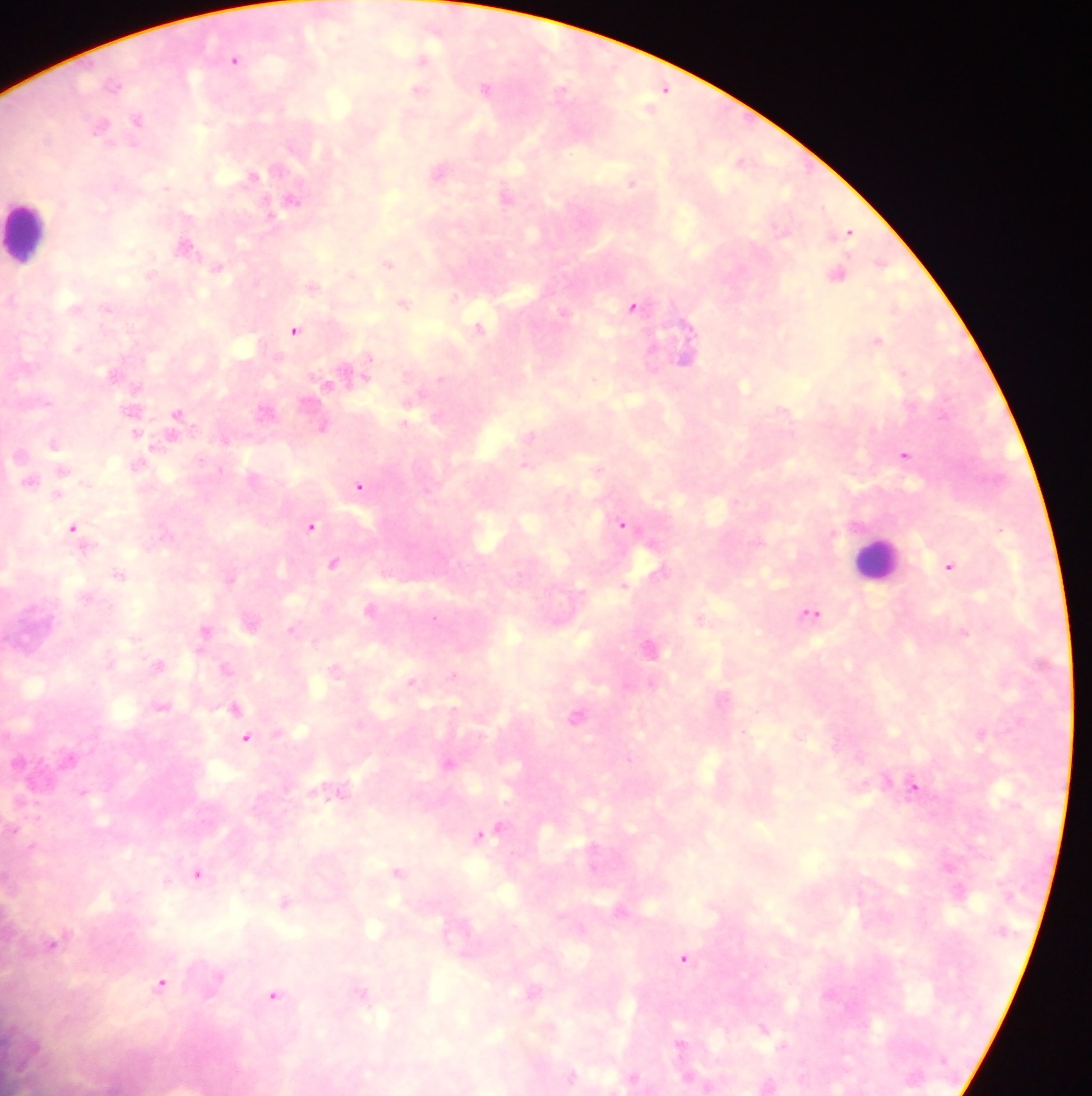
Approximate centers as [x, y] in pixels. Leukocyte locations: [25, 231], [877, 556]. Malaria parasite locations: [234, 59], [422, 60], [113, 84], [485, 88], [562, 89], [663, 89], [417, 90], [137, 119], [100, 125], [47, 138], [739, 161], [438, 171], [253, 175], [630, 183], [505, 196], [292, 199], [848, 232], [187, 246], [387, 263], [217, 268], [151, 274], [837, 274], [313, 285], [404, 303], [633, 306], [74, 307], [107, 308], [563, 312], [478, 326], [295, 330], [876, 340], [78, 348], [366, 362], [347, 372], [113, 374], [325, 384], [745, 386], [137, 388], [264, 410], [176, 414], [323, 427], [135, 433], [530, 435], [54, 444], [903, 454], [524, 465], [62, 471], [30, 481], [359, 486], [57, 495], [623, 524], [310, 526], [73, 528], [333, 562], [949, 566], [657, 570], [119, 575], [229, 579], [810, 614], [434, 617], [292, 629], [205, 630], [963, 632], [649, 647], [158, 665], [225, 668], [411, 680], [721, 698], [161, 706], [233, 708], [575, 715], [240, 718], [979, 733], [246, 738], [448, 763], [913, 787], [488, 832], [397, 872], [199, 875], [284, 902], [619, 909], [52, 944], [683, 959], [161, 983], [532, 991], [273, 996], [763, 1028], [678, 1044], [571, 1076], [633, 1077]. Sample from Ghana. One field of view. Image is 1092×1096 pixels. Thick blood film. Photographed through a microscope with a mobile-phone camera.